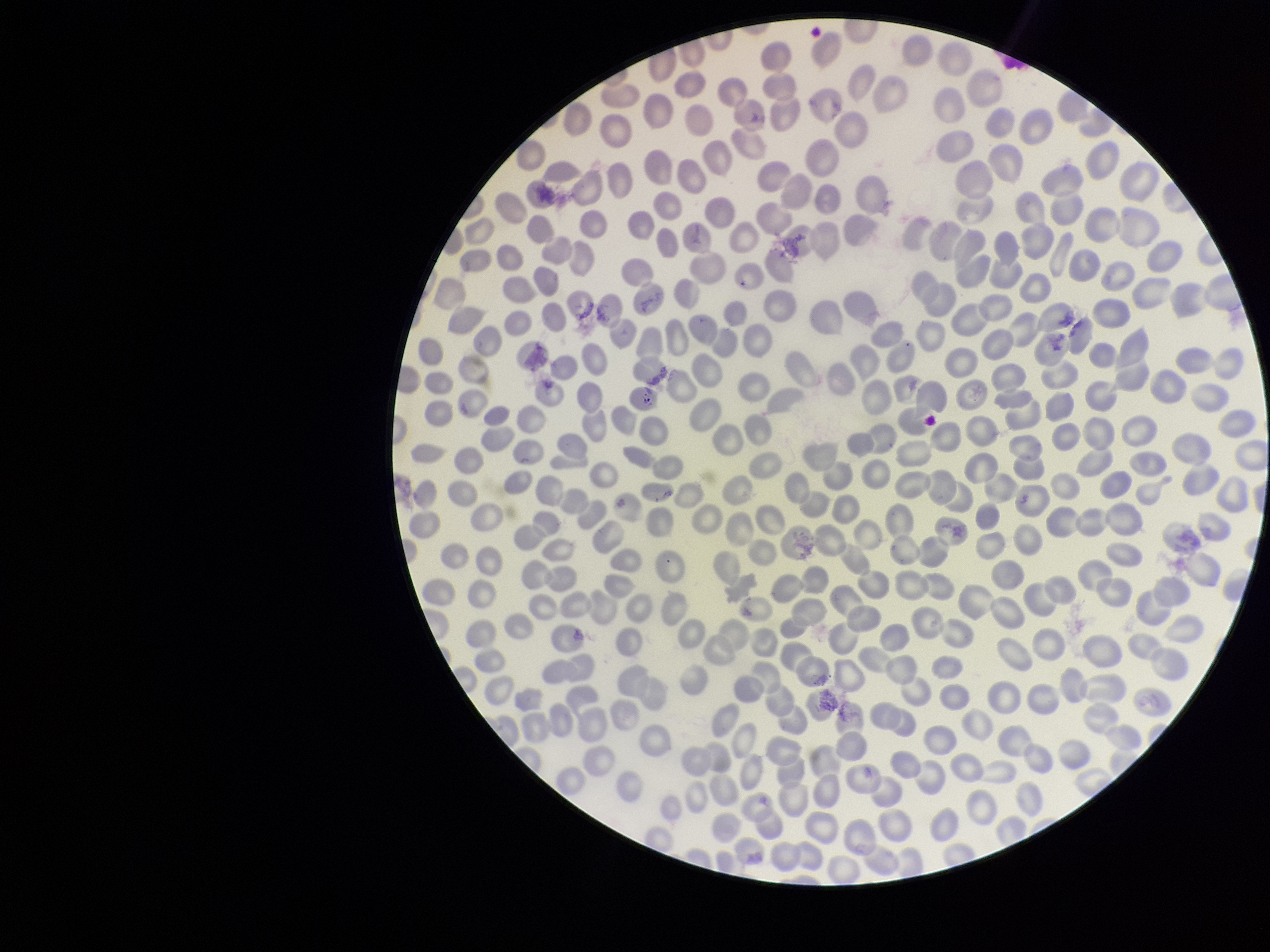

Red blood cell count: 318. Species reported for this patient: Plasmodium falciparum. Preparation: thin smear. Parasitized red blood cells: none seen. Patient malaria status: positive. Stained with Giemsa. Single field of view. Image is 1270×952 pixels. Parasitized red blood cell count: 0. Photographed through the microscope eyepiece with a smartphone camera.